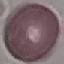
Result: no malaria parasites seen. Acquired by smartphone through the microscope eyepiece. Automatically extracted cell patch, resized to 64 × 64 pixels. Giemsa-stained preparation. Thin blood film.